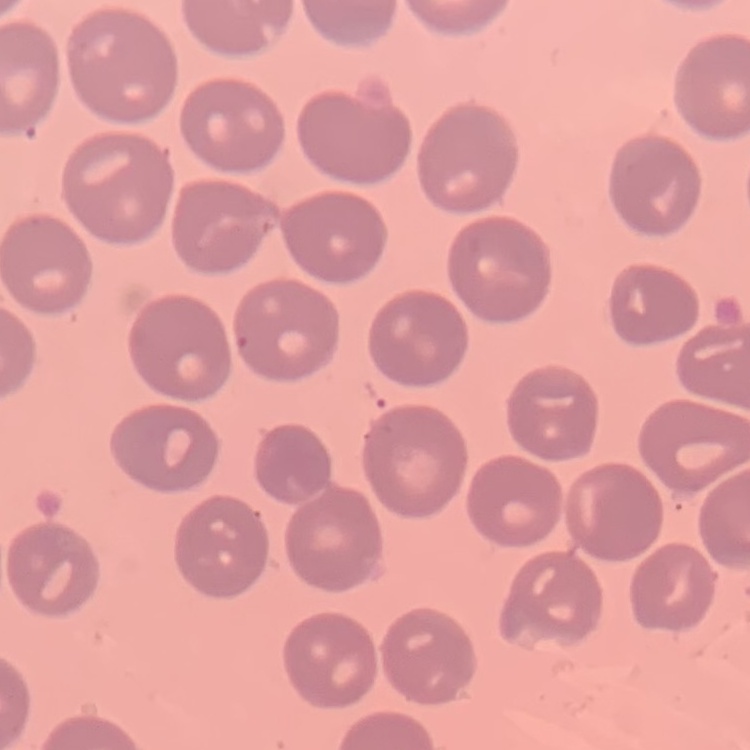 The erythrocytes show no rouleaux formation. Field's or Giemsa stain. Square crop of a larger photomicrograph. Thin blood film.